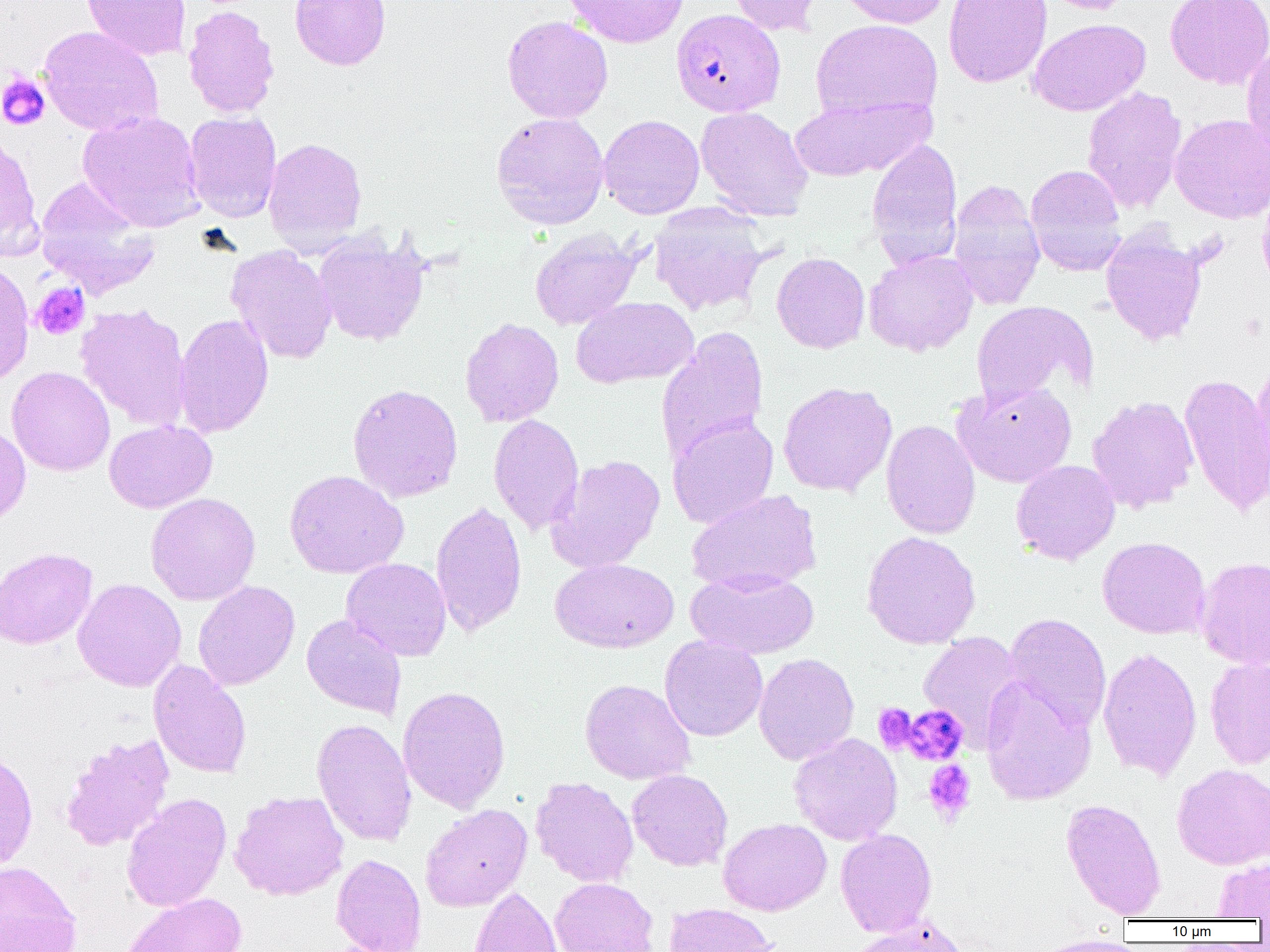

Summary:
  - Coordinate format: approximate bounding boxes as named x1/y1/x2/y2 corners in pixels
  - Platelet locations: (x1=0, y1=73, x2=50, y2=131), (x1=31, y1=282, x2=89, y2=340), (x1=873, y1=703, x2=919, y2=754), (x1=899, y1=704, x2=968, y2=765), (x1=922, y1=759, x2=976, y2=824)
  - Uninfected red blood cell locations: (x1=81, y1=0, x2=192, y2=61), (x1=290, y1=0, x2=391, y2=71), (x1=562, y1=0, x2=689, y2=48), (x1=725, y1=0, x2=824, y2=36), (x1=836, y1=0, x2=952, y2=28), (x1=943, y1=0, x2=1052, y2=88), (x1=1038, y1=0, x2=1136, y2=14), (x1=1165, y1=0, x2=1270, y2=89), (x1=182, y1=4, x2=280, y2=119), (x1=502, y1=15, x2=613, y2=123), (x1=810, y1=18, x2=943, y2=122), (x1=1028, y1=18, x2=1151, y2=116), (x1=37, y1=25, x2=164, y2=136), (x1=1241, y1=44, x2=1270, y2=162), (x1=1082, y1=86, x2=1187, y2=214), (x1=789, y1=94, x2=933, y2=181), (x1=695, y1=106, x2=814, y2=221), (x1=78, y1=110, x2=205, y2=231), (x1=184, y1=111, x2=282, y2=222), (x1=491, y1=111, x2=610, y2=229), (x1=1169, y1=113, x2=1270, y2=224), (x1=598, y1=114, x2=705, y2=219), (x1=0, y1=131, x2=42, y2=259), (x1=263, y1=137, x2=367, y2=252), (x1=866, y1=138, x2=964, y2=267), (x1=1024, y1=164, x2=1128, y2=276), (x1=34, y1=179, x2=160, y2=297), (x1=947, y1=179, x2=1045, y2=310), (x1=1257, y1=182, x2=1270, y2=297), (x1=649, y1=204, x2=770, y2=316), (x1=528, y1=228, x2=643, y2=330), (x1=1100, y1=228, x2=1208, y2=347), (x1=313, y1=231, x2=430, y2=347), (x1=226, y1=245, x2=338, y2=365), (x1=863, y1=250, x2=979, y2=356), (x1=771, y1=252, x2=870, y2=353), (x1=0, y1=260, x2=34, y2=385), (x1=571, y1=296, x2=698, y2=388), (x1=970, y1=300, x2=1097, y2=409), (x1=75, y1=303, x2=192, y2=432), (x1=173, y1=313, x2=274, y2=438), (x1=460, y1=317, x2=564, y2=426), (x1=473, y1=317, x2=570, y2=535), (x1=656, y1=326, x2=769, y2=463), (x1=1248, y1=360, x2=1270, y2=499), (x1=6, y1=366, x2=115, y2=476), (x1=1179, y1=371, x2=1270, y2=517), (x1=778, y1=381, x2=897, y2=497), (x1=953, y1=381, x2=1077, y2=488), (x1=347, y1=383, x2=463, y2=503), (x1=1087, y1=395, x2=1199, y2=513), (x1=488, y1=413, x2=584, y2=535), (x1=668, y1=414, x2=778, y2=529), (x1=881, y1=419, x2=981, y2=539), (x1=104, y1=420, x2=217, y2=513), (x1=0, y1=422, x2=31, y2=530), (x1=547, y1=454, x2=666, y2=573), (x1=1011, y1=460, x2=1121, y2=565), (x1=284, y1=470, x2=409, y2=579), (x1=686, y1=490, x2=822, y2=594), (x1=145, y1=492, x2=261, y2=605), (x1=431, y1=501, x2=527, y2=636), (x1=861, y1=530, x2=981, y2=649), (x1=1098, y1=537, x2=1210, y2=639), (x1=0, y1=547, x2=98, y2=649), (x1=1196, y1=556, x2=1270, y2=669), (x1=341, y1=557, x2=452, y2=661), (x1=550, y1=559, x2=679, y2=653), (x1=686, y1=569, x2=819, y2=659), (x1=73, y1=578, x2=186, y2=691), (x1=193, y1=581, x2=299, y2=690), (x1=1004, y1=612, x2=1112, y2=733), (x1=301, y1=614, x2=407, y2=720), (x1=918, y1=631, x2=1025, y2=747), (x1=659, y1=635, x2=768, y2=742), (x1=1098, y1=647, x2=1202, y2=781), (x1=753, y1=653, x2=859, y2=765), (x1=1204, y1=657, x2=1270, y2=768), (x1=148, y1=660, x2=252, y2=779), (x1=979, y1=677, x2=1096, y2=806), (x1=579, y1=678, x2=696, y2=785), (x1=397, y1=685, x2=511, y2=813), (x1=311, y1=718, x2=417, y2=847), (x1=789, y1=732, x2=903, y2=845), (x1=60, y1=733, x2=175, y2=851), (x1=0, y1=746, x2=38, y2=872), (x1=1172, y1=763, x2=1270, y2=869), (x1=627, y1=769, x2=733, y2=871), (x1=530, y1=777, x2=639, y2=887), (x1=229, y1=790, x2=349, y2=900), (x1=121, y1=793, x2=232, y2=912), (x1=1060, y1=798, x2=1166, y2=919), (x1=420, y1=804, x2=533, y2=911), (x1=718, y1=818, x2=832, y2=916), (x1=835, y1=828, x2=937, y2=936), (x1=331, y1=853, x2=426, y2=952), (x1=1212, y1=857, x2=1270, y2=919), (x1=0, y1=860, x2=81, y2=952), (x1=550, y1=877, x2=659, y2=952), (x1=469, y1=885, x2=562, y2=952), (x1=121, y1=892, x2=247, y2=952), (x1=663, y1=903, x2=778, y2=952), (x1=849, y1=918, x2=970, y2=952), (x1=1030, y1=937, x2=1143, y2=952)
  - Plasmodium falciparum-infected red blood cell locations: (x1=671, y1=8, x2=785, y2=117)
  - Slide-level diagnosis: Plasmodium falciparum
  - Image size: 1270×952 pixels
  - Field of view: one of a larger specimen
  - Modality: optical microscopy
  - Magnification: 1000x
  - Preparation: thin blood film